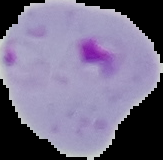
result: Plasmodium parasites detected
image_size: 163×160 pixels
preparation: thin blood smear
image_type: segmented cell region with the area outside set to black